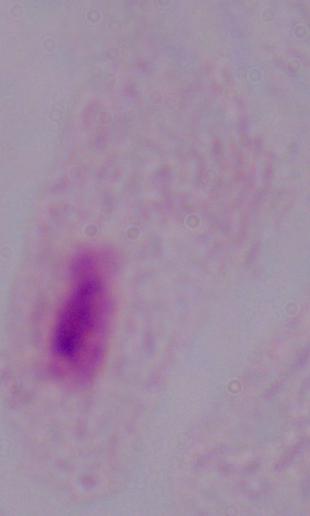
Summary:
  - Modality: photomicrograph
  - Magnification: 1000x
  - Identification: trichomonad